Report the malaria status of this cell.
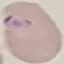
It is parasitized.

Summary:
  - Stain: Giemsa
  - Image type: cell patch, automatically extracted from a larger field of view and resized to 64 × 64 pixels
  - Preparation: thin smear
  - Capture: smartphone through the microscope eyepiece